Locate every malaria parasite and every leukocyte.
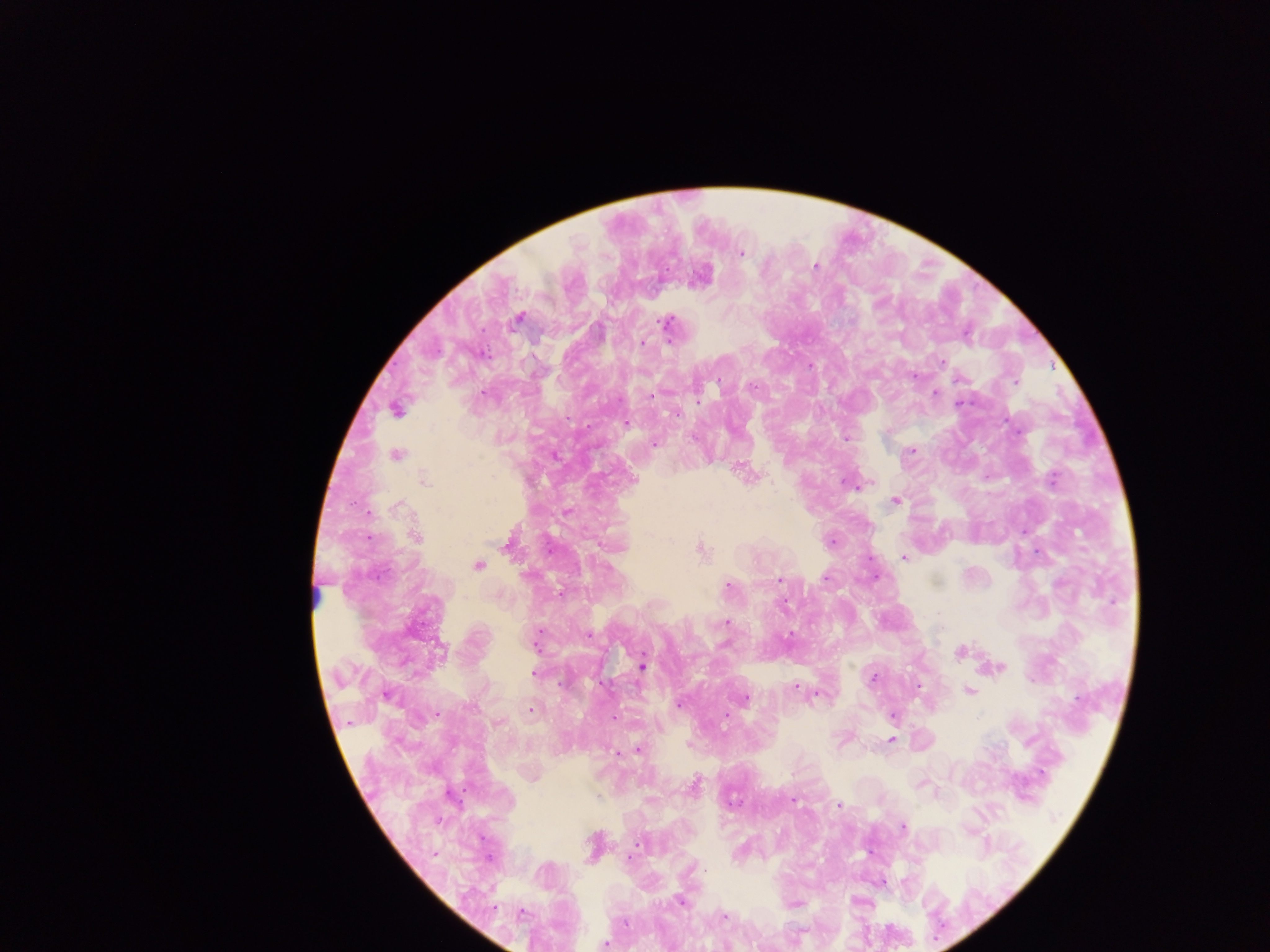
Approximate centers as [x, y] in pixels.
Malaria parasites: [741, 253], [814, 267], [518, 317], [665, 323], [643, 342], [942, 362], [810, 366], [1015, 381], [752, 386], [935, 393], [650, 396], [698, 399], [959, 404], [396, 410], [676, 413], [626, 424], [693, 438], [653, 444], [911, 450], [396, 454], [555, 455], [1053, 479], [425, 481], [851, 484], [895, 500], [398, 505], [415, 537], [831, 542], [702, 550], [903, 558], [477, 565], [825, 578], [780, 579], [728, 587], [726, 623], [588, 635], [789, 635], [535, 643], [441, 650], [959, 653], [642, 666], [999, 667], [534, 674], [873, 678], [918, 685], [795, 688], [969, 690], [817, 694], [387, 697], [745, 699], [680, 705], [531, 711], [891, 716], [614, 718], [498, 723], [891, 738], [638, 750], [618, 754], [695, 784], [597, 797], [793, 800], [838, 806], [903, 828], [638, 846], [630, 857], [703, 869], [680, 902], [522, 912], [724, 917], [624, 922], [604, 944].
Leukocytes: [314, 596].

Summary:
  - Field of view: single
  - Country: Ghana
  - Image size: 1270×952 pixels
  - Capture: mobile-phone photograph through a microscope
  - Preparation: thick blood film